Identify the preparation type.
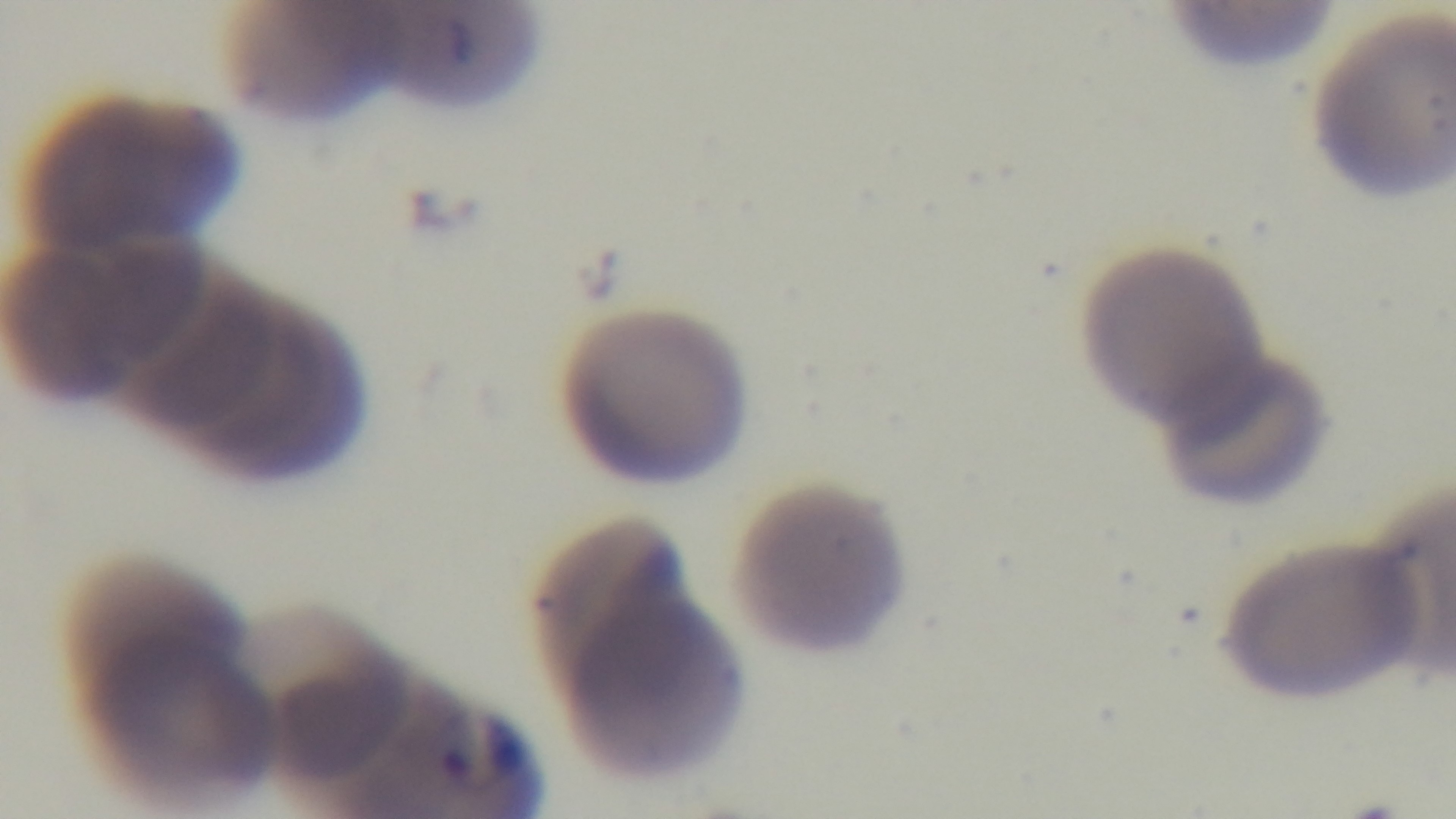

A thin smear.

Light microscopy. Malaria status: positive. Giemsa-stained. Single field of view. Mounted 4K digital camera. 100x oil-immersion objective.